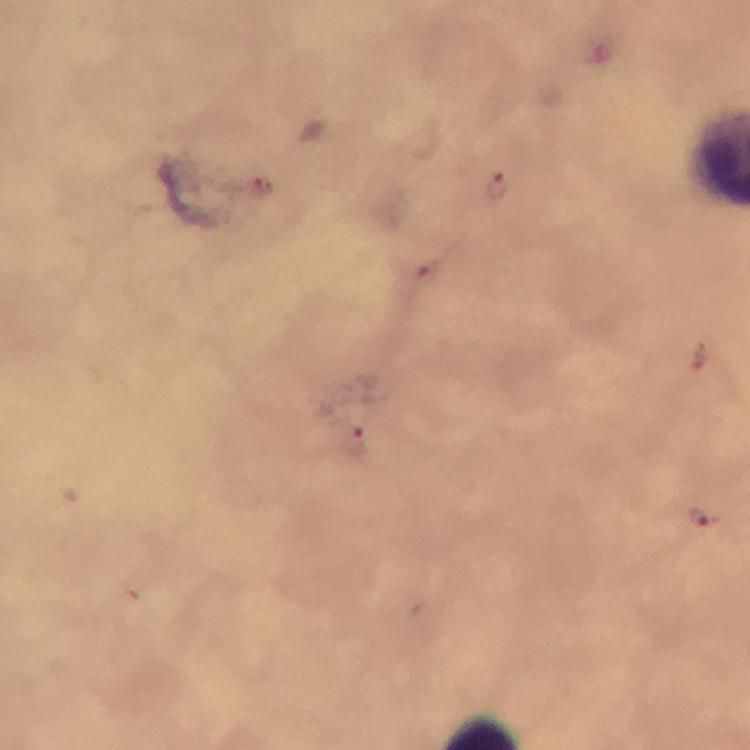
context = from a malaria diagnostic workup
immersion oil = applied
magnification = 100x
stain = Giemsa
image size = 750×750 pixels
cropped from = a single field of view
preparation = thick blood smear
Plasmodium parasite locations = approximate object centers, in pixels from the top-left corner: (x=260, y=188), (x=497, y=188), (x=426, y=282), (x=697, y=358), (x=355, y=440), (x=700, y=518)
capture = smartphone photograph through a microscope